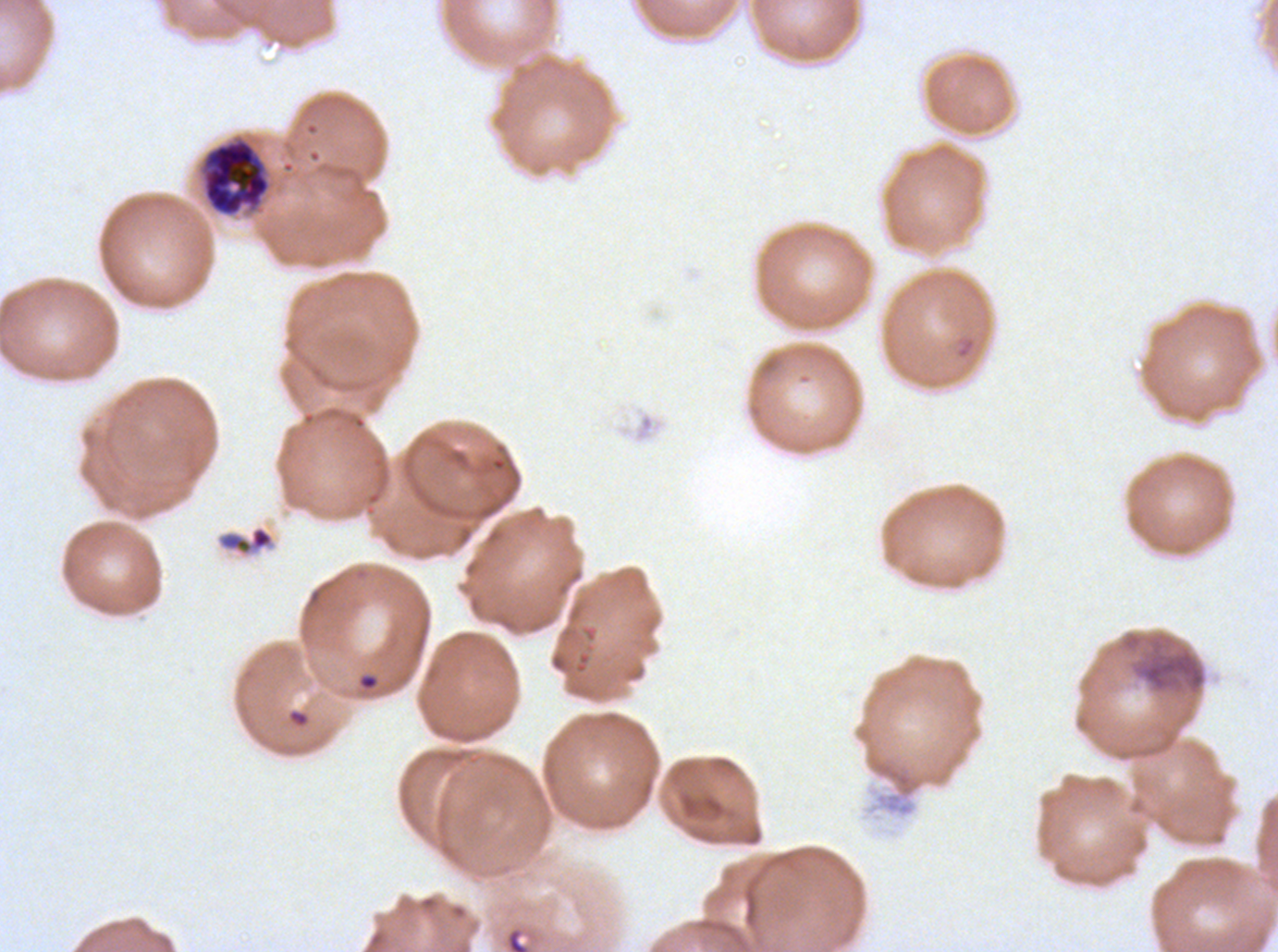

Approximate bounding boxes as (x1, y1, x2, y2) in pixels. Ring locations: (358, 674, 379, 690), (287, 709, 310, 727), (505, 927, 530, 951). Debris locations: (218, 526, 274, 555), (1119, 630, 1208, 698). Early schizont locations: (204, 140, 269, 214). Image is 1278×952 pixels. One sub-image of a larger composite. Thin blood smear. Life-cycle stages observed: ring, early schizont. Plasmodium falciparum from a patient in The Gambia, cultured ex vivo for 24 to 48 hours. Giemsa stain.